Assess this cell for malaria.
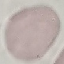

Uninfected.

stain = Giemsa
capture = smartphone camera at the microscope eyepiece
image type = automatically extracted cell patch, resized to 64 × 64 pixels
preparation = thin blood smear